Comment on the morphology of the erythrocytes.
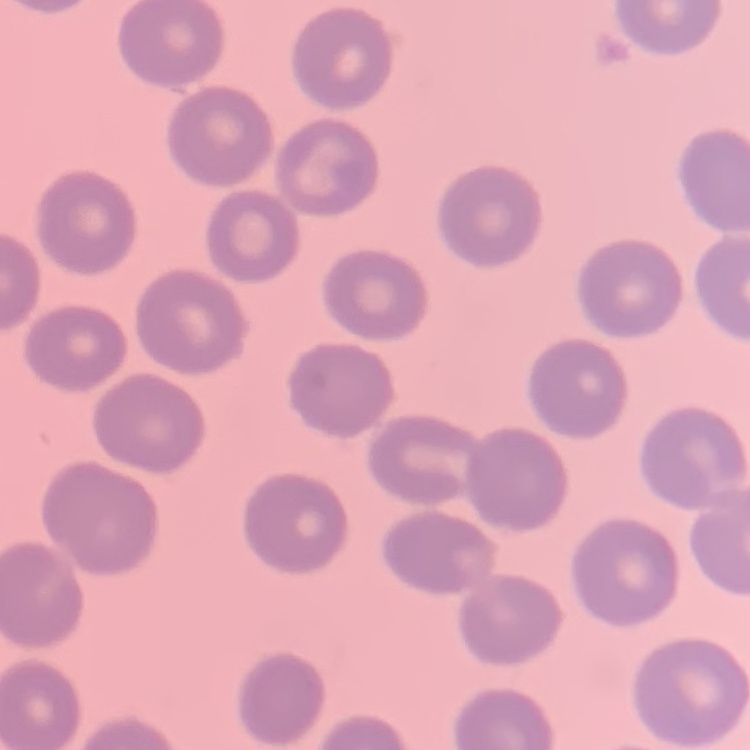
No rouleaux formation.

Square crop of a larger photomicrograph. Thin peripheral smear. Field's or Giemsa stain.